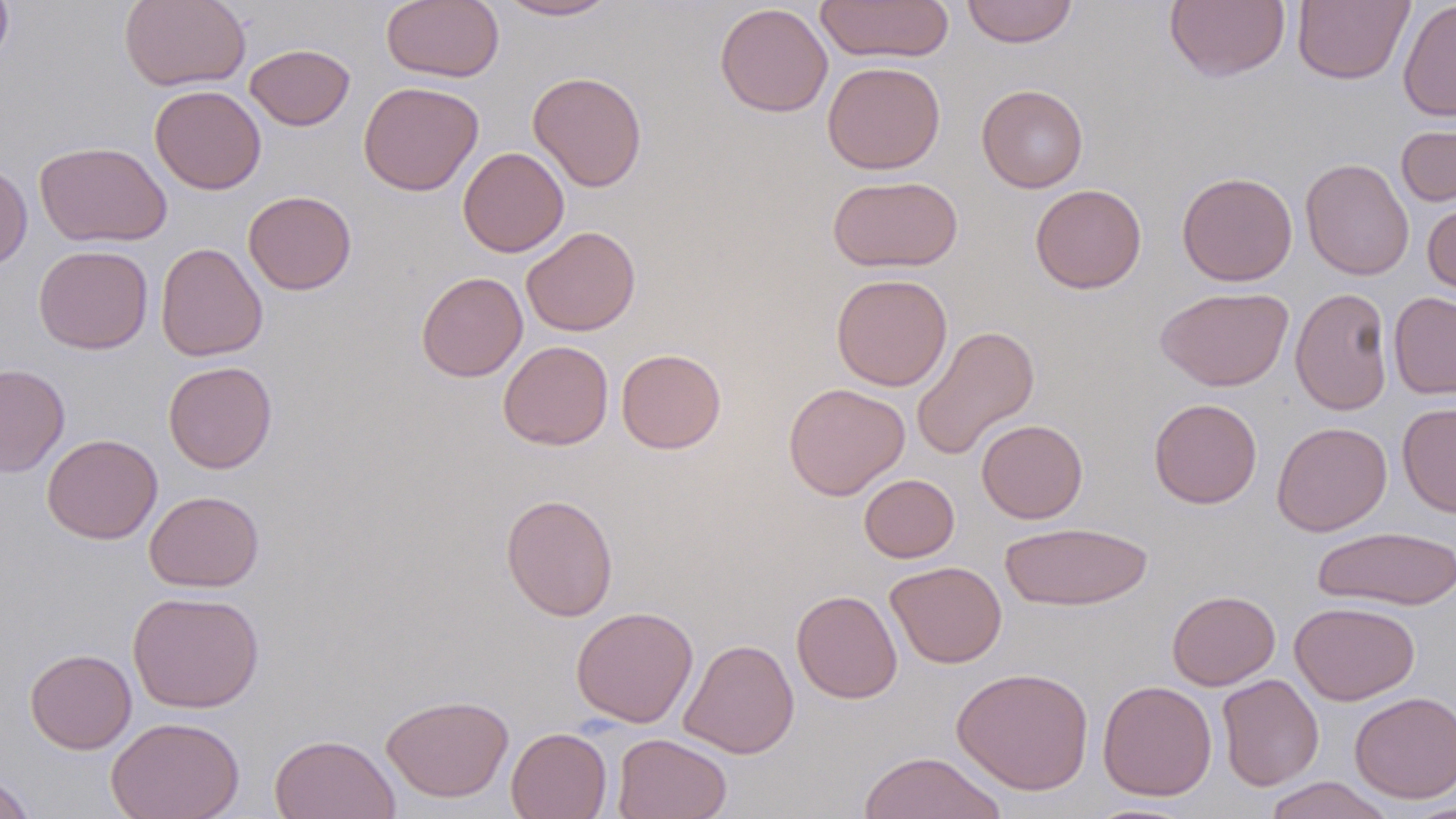
Summary:
  - Coordinate format: approximate bounding boxes as named x1/y1/x2/y2 corners in pixels
  - Uninfected red blood cell locations: (x1=0, y1=0, x2=13, y2=71), (x1=119, y1=0, x2=250, y2=91), (x1=381, y1=0, x2=504, y2=83), (x1=496, y1=0, x2=620, y2=21), (x1=814, y1=0, x2=955, y2=64), (x1=961, y1=0, x2=1078, y2=48), (x1=1164, y1=0, x2=1290, y2=83), (x1=1292, y1=0, x2=1414, y2=85), (x1=1397, y1=0, x2=1456, y2=121), (x1=714, y1=3, x2=833, y2=117), (x1=244, y1=43, x2=355, y2=131), (x1=822, y1=61, x2=945, y2=174), (x1=528, y1=70, x2=648, y2=192), (x1=359, y1=81, x2=483, y2=196), (x1=150, y1=85, x2=266, y2=194), (x1=976, y1=85, x2=1088, y2=193), (x1=1395, y1=122, x2=1456, y2=207), (x1=34, y1=141, x2=172, y2=248), (x1=458, y1=147, x2=569, y2=257), (x1=1300, y1=158, x2=1414, y2=280), (x1=0, y1=162, x2=32, y2=270), (x1=1177, y1=171, x2=1298, y2=286), (x1=827, y1=174, x2=963, y2=273), (x1=1029, y1=184, x2=1147, y2=294), (x1=243, y1=190, x2=357, y2=295), (x1=1422, y1=197, x2=1456, y2=300), (x1=521, y1=226, x2=641, y2=336), (x1=155, y1=242, x2=268, y2=362), (x1=34, y1=244, x2=153, y2=354), (x1=416, y1=271, x2=527, y2=382), (x1=831, y1=273, x2=952, y2=391), (x1=1290, y1=286, x2=1393, y2=416), (x1=1155, y1=287, x2=1294, y2=392), (x1=1388, y1=291, x2=1456, y2=399), (x1=911, y1=325, x2=1040, y2=460), (x1=498, y1=340, x2=614, y2=451), (x1=616, y1=348, x2=726, y2=454), (x1=163, y1=360, x2=277, y2=473), (x1=0, y1=363, x2=70, y2=477), (x1=783, y1=382, x2=910, y2=500), (x1=1148, y1=398, x2=1262, y2=509), (x1=1397, y1=402, x2=1456, y2=518), (x1=976, y1=419, x2=1088, y2=524), (x1=1271, y1=421, x2=1392, y2=536), (x1=42, y1=433, x2=163, y2=544), (x1=859, y1=473, x2=959, y2=562), (x1=144, y1=490, x2=264, y2=592), (x1=500, y1=493, x2=619, y2=621), (x1=1000, y1=521, x2=1153, y2=611), (x1=1312, y1=526, x2=1456, y2=610), (x1=885, y1=561, x2=1007, y2=669), (x1=791, y1=589, x2=902, y2=703), (x1=1167, y1=590, x2=1281, y2=690), (x1=127, y1=591, x2=264, y2=713), (x1=1289, y1=601, x2=1420, y2=705), (x1=570, y1=605, x2=698, y2=727), (x1=679, y1=639, x2=799, y2=758), (x1=25, y1=648, x2=136, y2=754), (x1=952, y1=666, x2=1094, y2=795), (x1=1217, y1=673, x2=1324, y2=791), (x1=1097, y1=679, x2=1217, y2=801), (x1=1350, y1=691, x2=1455, y2=803), (x1=380, y1=694, x2=514, y2=802), (x1=106, y1=716, x2=245, y2=819), (x1=506, y1=726, x2=612, y2=819), (x1=269, y1=733, x2=400, y2=819), (x1=612, y1=733, x2=732, y2=819), (x1=857, y1=751, x2=1007, y2=819), (x1=0, y1=770, x2=38, y2=818), (x1=1261, y1=776, x2=1396, y2=819), (x1=1081, y1=801, x2=1201, y2=818), (x1=1402, y1=802, x2=1456, y2=818)
  - Slide-level diagnosis: no evidence of blood parasites
  - Stain: May-Grünwald-Giemsa
  - Magnification: 1000x
  - Field of view: single
  - Modality: light microscopy
  - Image size: 1456×819 pixels
  - Preparation: thin blood smear